Report the malaria status of this cell.
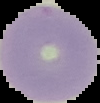

Uninfected.

Summary:
  - Preparation: thin blood smear
  - Image size: 100×103 pixels
  - Image type: segmented cell region with the area outside set to black